Classify this cell by malaria status.
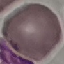

It is uninfected.

image type = automatically extracted cell patch, resized to 64 × 64 pixels
preparation = thin smear
capture = smartphone through the microscope eyepiece
stain = Giemsa